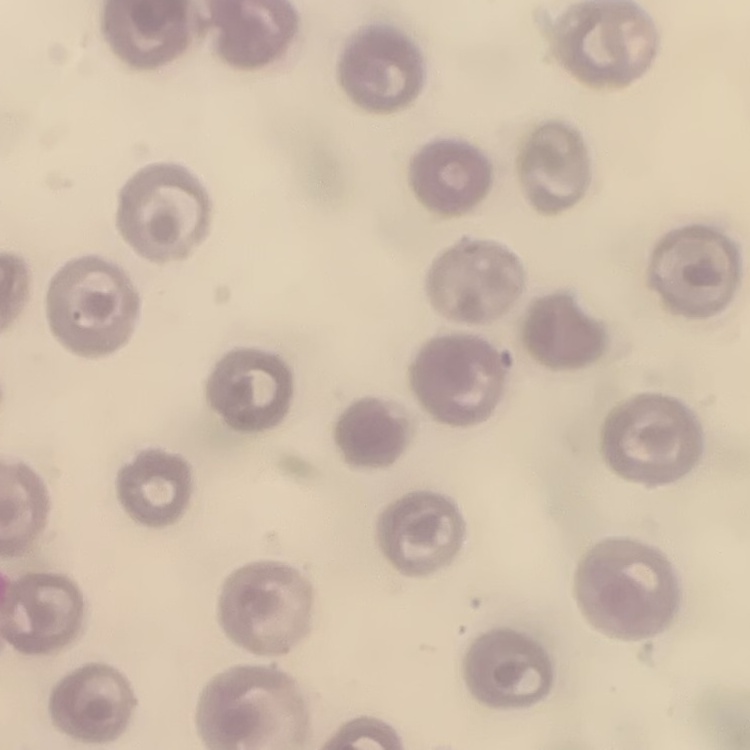
Summary:
  - Erythrocyte morphology: no rouleaux formation
  - Stain: Field's or Giemsa
  - Preparation: thin blood film
  - Image type: square crop of a larger photomicrograph